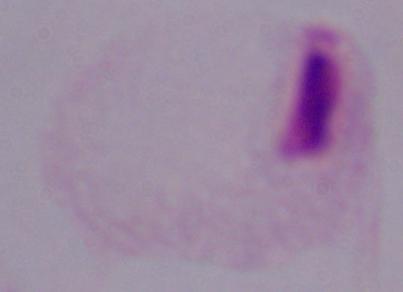
Summary:
  - Modality: photomicrograph
  - Identification: trichomonad
  - Magnification: 1000x